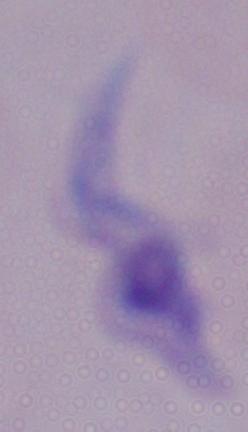
Summary:
  - Modality: photomicrograph
  - Magnification: 1000x
  - Identification: trypanosome